State the blood parasite species.
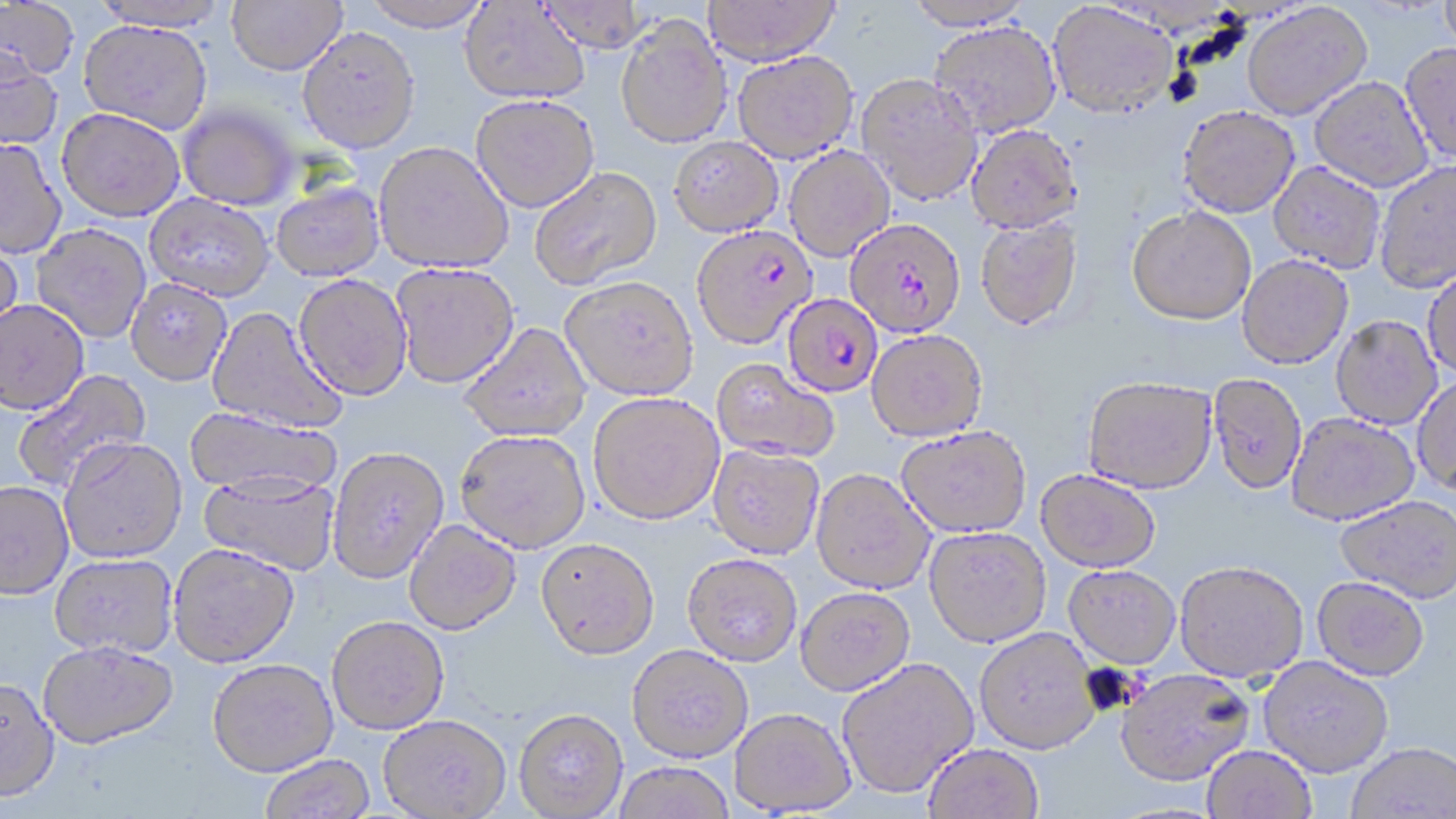
Plasmodium falciparum.

Approximate bounding boxes as named x1/y1/x2/y2 corners in pixels. Uninfected red blood cell locations: (x1=0, y1=0, x2=80, y2=83), (x1=90, y1=0, x2=232, y2=32), (x1=226, y1=0, x2=347, y2=75), (x1=362, y1=0, x2=493, y2=32), (x1=536, y1=0, x2=648, y2=54), (x1=703, y1=0, x2=840, y2=65), (x1=903, y1=0, x2=1034, y2=30), (x1=1439, y1=0, x2=1456, y2=55), (x1=459, y1=2, x2=589, y2=104), (x1=1047, y1=2, x2=1178, y2=118), (x1=1241, y1=3, x2=1372, y2=120), (x1=615, y1=15, x2=731, y2=149), (x1=78, y1=19, x2=214, y2=135), (x1=928, y1=21, x2=1061, y2=138), (x1=297, y1=26, x2=420, y2=153), (x1=1400, y1=42, x2=1456, y2=164), (x1=0, y1=49, x2=64, y2=150), (x1=732, y1=49, x2=859, y2=163), (x1=856, y1=73, x2=983, y2=206), (x1=1309, y1=76, x2=1433, y2=192), (x1=470, y1=93, x2=600, y2=213), (x1=177, y1=105, x2=300, y2=210), (x1=1178, y1=105, x2=1299, y2=217), (x1=57, y1=107, x2=185, y2=221), (x1=966, y1=124, x2=1082, y2=233), (x1=669, y1=136, x2=784, y2=236), (x1=0, y1=138, x2=67, y2=259), (x1=374, y1=141, x2=513, y2=273), (x1=783, y1=146, x2=895, y2=261), (x1=1373, y1=160, x2=1456, y2=293), (x1=1269, y1=161, x2=1386, y2=274), (x1=529, y1=166, x2=661, y2=289), (x1=270, y1=182, x2=384, y2=281), (x1=145, y1=193, x2=275, y2=301), (x1=1127, y1=205, x2=1256, y2=325), (x1=974, y1=217, x2=1083, y2=331), (x1=31, y1=224, x2=151, y2=343), (x1=0, y1=237, x2=24, y2=349), (x1=1237, y1=254, x2=1353, y2=369), (x1=390, y1=262, x2=520, y2=388), (x1=1422, y1=265, x2=1456, y2=378), (x1=293, y1=274, x2=412, y2=400), (x1=561, y1=275, x2=699, y2=400), (x1=126, y1=278, x2=232, y2=385), (x1=0, y1=298, x2=90, y2=414), (x1=207, y1=306, x2=347, y2=436), (x1=1331, y1=315, x2=1442, y2=430), (x1=459, y1=322, x2=591, y2=442), (x1=867, y1=329, x2=988, y2=441), (x1=712, y1=358, x2=839, y2=461), (x1=12, y1=369, x2=152, y2=493), (x1=1208, y1=372, x2=1308, y2=495), (x1=1412, y1=374, x2=1456, y2=494), (x1=1082, y1=375, x2=1218, y2=493), (x1=587, y1=391, x2=725, y2=525), (x1=184, y1=407, x2=341, y2=499), (x1=1286, y1=413, x2=1420, y2=525), (x1=896, y1=426, x2=1031, y2=538), (x1=455, y1=429, x2=590, y2=552), (x1=59, y1=437, x2=187, y2=562), (x1=708, y1=444, x2=825, y2=559), (x1=327, y1=446, x2=449, y2=584), (x1=811, y1=468, x2=935, y2=595), (x1=1035, y1=469, x2=1161, y2=572), (x1=198, y1=471, x2=340, y2=576), (x1=0, y1=480, x2=74, y2=599), (x1=1335, y1=495, x2=1456, y2=602), (x1=403, y1=520, x2=522, y2=635), (x1=923, y1=525, x2=1052, y2=647), (x1=536, y1=537, x2=659, y2=659), (x1=168, y1=543, x2=299, y2=667), (x1=682, y1=552, x2=802, y2=666), (x1=50, y1=553, x2=179, y2=658), (x1=1175, y1=559, x2=1309, y2=683), (x1=1063, y1=564, x2=1181, y2=668), (x1=1311, y1=576, x2=1429, y2=681), (x1=795, y1=586, x2=915, y2=696), (x1=326, y1=615, x2=449, y2=734), (x1=974, y1=627, x2=1101, y2=755), (x1=37, y1=640, x2=178, y2=749), (x1=627, y1=643, x2=753, y2=762), (x1=836, y1=656, x2=979, y2=799), (x1=1258, y1=656, x2=1393, y2=777), (x1=207, y1=658, x2=338, y2=776), (x1=1115, y1=668, x2=1254, y2=786), (x1=0, y1=677, x2=60, y2=802), (x1=513, y1=708, x2=628, y2=818), (x1=729, y1=708, x2=855, y2=815), (x1=378, y1=715, x2=511, y2=818), (x1=1347, y1=742, x2=1456, y2=818), (x1=922, y1=743, x2=1043, y2=819), (x1=1202, y1=745, x2=1317, y2=819), (x1=259, y1=754, x2=375, y2=819), (x1=613, y1=762, x2=734, y2=819). Plasmodium falciparum-infected red blood cell locations: (x1=845, y1=217, x2=966, y2=338), (x1=691, y1=225, x2=817, y2=349), (x1=783, y1=294, x2=884, y2=397). Light microscopy. Image is 1456×819 pixels. Single field of view. May-Grünwald-Giemsa-stained preparation. 1000x magnification. Thin blood film.